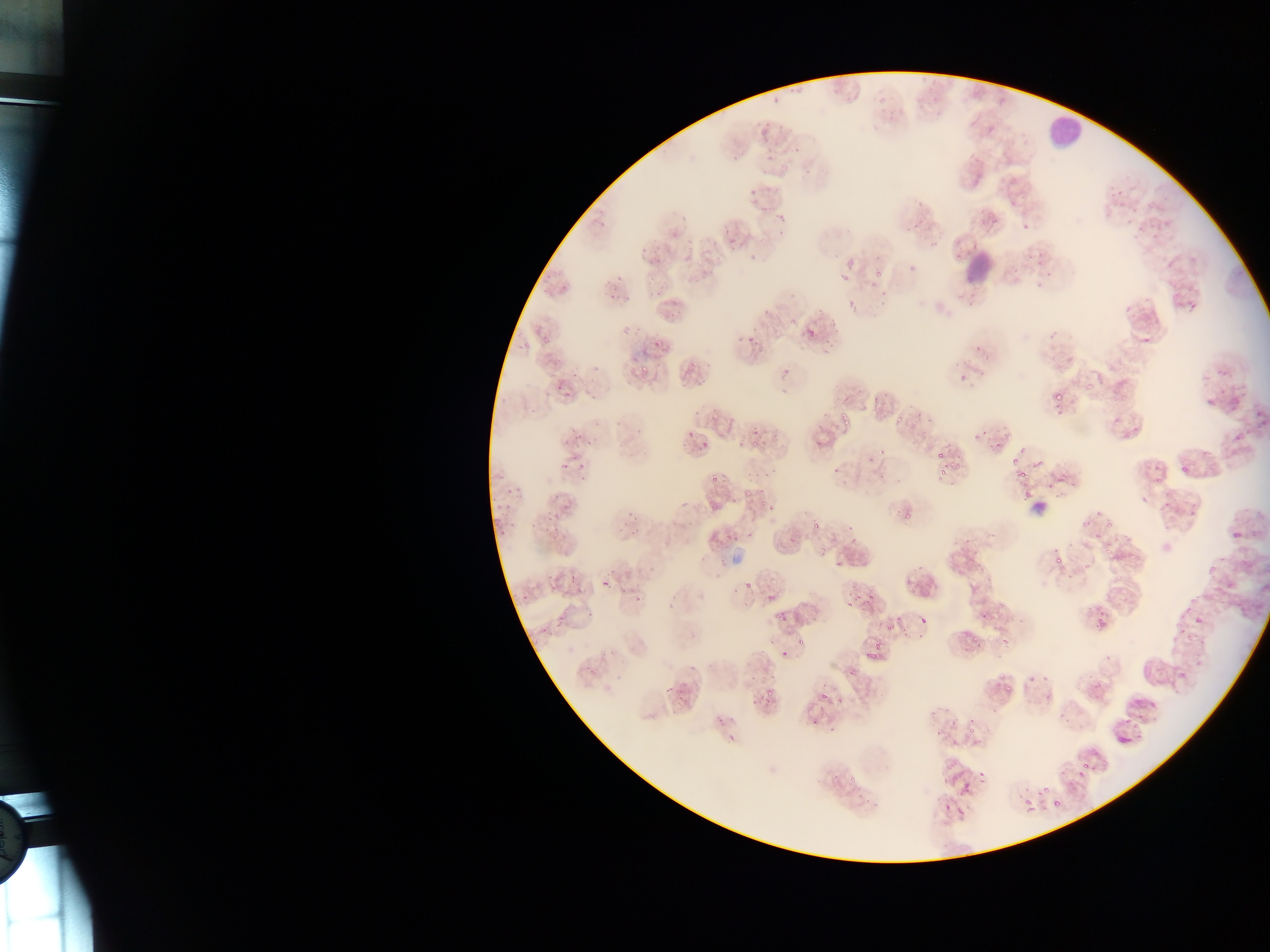

Approximate bounding boxes as (left, top, right, bottom) in pixels. Leukocyte locations: (1044, 121, 1087, 149), (1025, 504, 1050, 521). Malaria parasite locations: (772, 97, 779, 108), (757, 116, 766, 128), (766, 148, 776, 160), (732, 151, 741, 162), (986, 212, 995, 220), (780, 215, 789, 225), (953, 233, 964, 243), (750, 249, 759, 260), (872, 270, 885, 278), (649, 271, 660, 282), (837, 272, 849, 284), (616, 274, 622, 283), (973, 279, 985, 293), (655, 287, 664, 296), (609, 294, 618, 301), (669, 303, 678, 316), (787, 317, 797, 326), (807, 323, 816, 334), (747, 330, 759, 344), (1143, 337, 1151, 346), (651, 339, 662, 353), (660, 350, 671, 357), (641, 363, 650, 373), (573, 369, 579, 380), (553, 378, 574, 401), (696, 378, 705, 387), (1085, 382, 1095, 393), (1049, 385, 1063, 405), (1121, 394, 1130, 402), (872, 396, 882, 404), (729, 411, 742, 424), (894, 415, 902, 421), (839, 416, 851, 427), (683, 430, 696, 439), (972, 430, 981, 445), (1005, 430, 1012, 440), (575, 431, 584, 443), (750, 438, 761, 447), (735, 440, 742, 449), (698, 442, 711, 451), (585, 443, 594, 447), (993, 444, 1002, 452), (879, 445, 893, 457), (934, 447, 947, 460), (575, 458, 589, 470), (1015, 459, 1032, 481), (559, 461, 572, 470), (954, 461, 963, 474), (1180, 464, 1191, 474), (939, 466, 948, 477), (710, 470, 717, 484), (1039, 471, 1048, 480), (721, 476, 729, 487), (505, 482, 515, 493), (742, 483, 755, 496), (551, 487, 565, 504), (704, 492, 711, 502), (760, 497, 770, 508), (504, 498, 513, 513), (902, 508, 913, 521), (635, 511, 645, 522), (547, 514, 553, 523), (1081, 514, 1090, 528), (810, 515, 827, 529), (1105, 519, 1113, 530), (498, 524, 511, 540), (553, 524, 563, 534), (627, 528, 638, 537), (1230, 530, 1242, 539), (722, 531, 731, 542), (1105, 543, 1116, 555), (815, 549, 830, 558), (1054, 555, 1063, 564), (835, 556, 844, 566), (1081, 564, 1089, 574), (546, 570, 556, 579), (569, 571, 577, 583), (598, 573, 608, 588), (744, 580, 752, 590), (521, 591, 528, 600), (634, 591, 643, 602), (765, 592, 776, 604), (851, 593, 863, 601), (868, 593, 877, 600), (997, 597, 1005, 607), (846, 603, 855, 610), (585, 606, 595, 618), (1088, 607, 1110, 629), (772, 610, 787, 622), (559, 612, 568, 622), (919, 613, 928, 623), (987, 615, 995, 622), (885, 625, 894, 634), (971, 631, 980, 644), (1000, 631, 1013, 649), (795, 632, 807, 646), (781, 652, 788, 661), (864, 653, 875, 661), (850, 667, 855, 677), (995, 677, 1005, 688), (663, 681, 674, 694), (764, 686, 775, 696), (820, 687, 829, 702), (765, 693, 774, 708), (717, 715, 729, 728), (811, 715, 823, 729), (968, 721, 978, 733) | approximate (x, y) pixel centers of objects too small to bound: (796, 149), (807, 170), (753, 191), (835, 470), (898, 619), (543, 630), (878, 647), (752, 701), (832, 729). Single field of view. Collected in Ghana. Photographed through a microscope with a mobile-phone camera. Image is 1270×952 pixels. Thin blood film.